State which parasite is depicted.
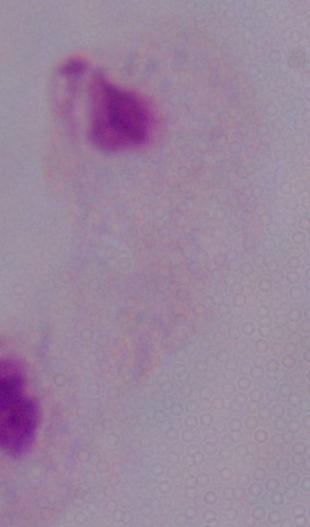

A trichomonad.

{
  "magnification": "1000x",
  "modality": "micrograph"
}